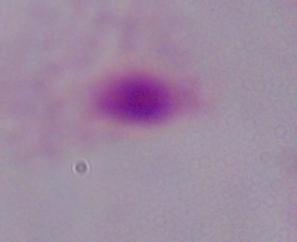
Summary:
  - Magnification: 1000x
  - Identification: trichomonad
  - Modality: micrograph